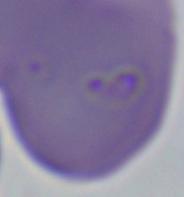

identification = Babesia
magnification = 1000x
modality = micrograph